Describe the morphology of the erythrocytes.
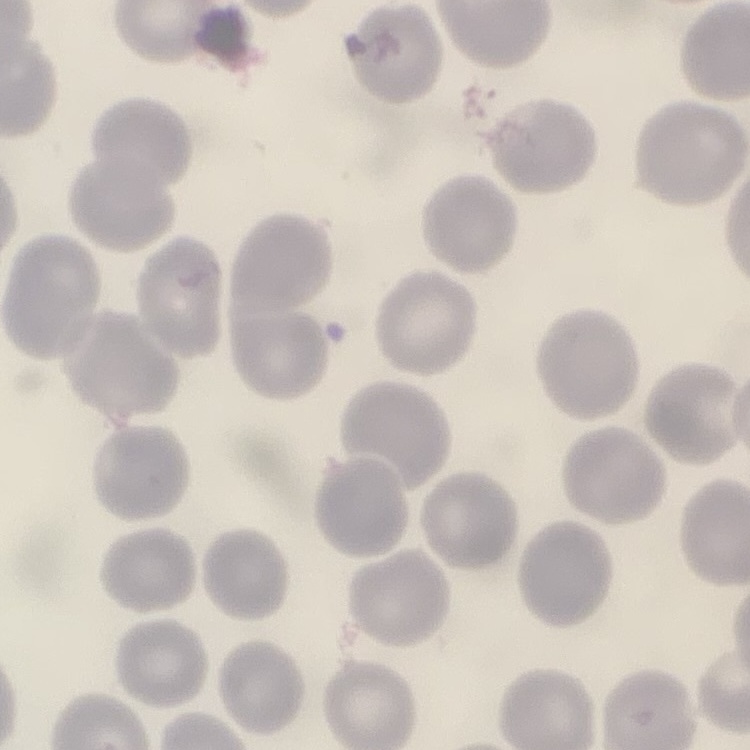

No rouleaux formation.

Summary:
  - Image type: one tile cut from a larger photomicrograph
  - Stain: Field's or Giemsa
  - Preparation: thin blood film